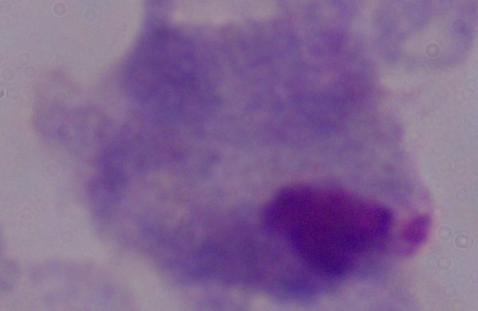
{
  "modality": "photomicrograph",
  "identification": "trichomonad",
  "magnification": "1000x"
}